Locate and identify every blood parasite.
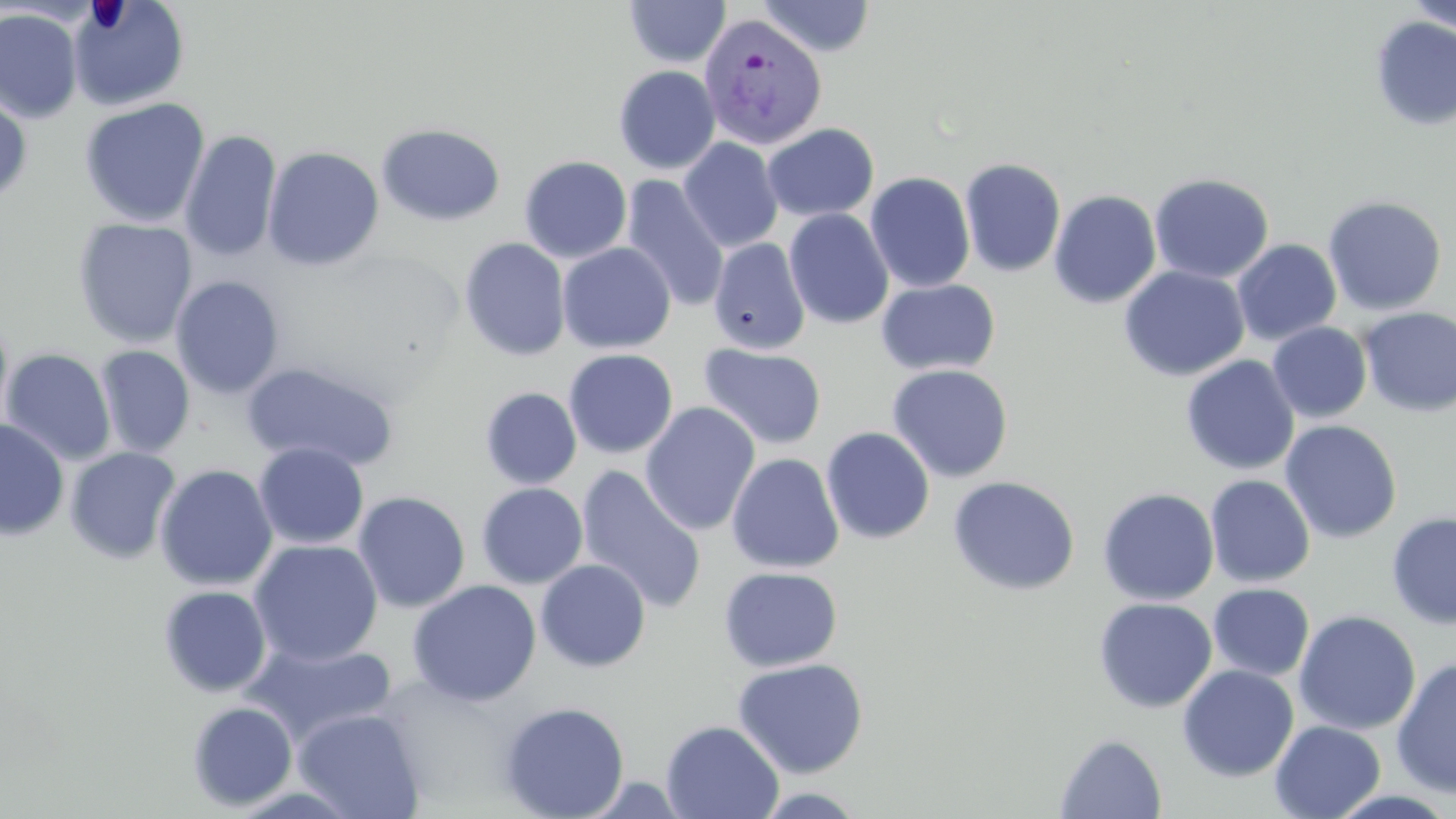
Approximate bounding boxes as (x1, y1, x2, y2) in pixels.
Plasmodium vivax-infected red blood cells: (699, 13, 828, 150).
No Plasmodium falciparum, Plasmodium ovale, Plasmodium malariae, Babesia divergens, or Trypanosoma brucei observed.

{
  "slide_level_diagnosis": "Plasmodium vivax",
  "magnification": "1000x",
  "modality": "optical microscopy",
  "uninfected_red_blood_cell_locations": "approximate bounding boxes as (x1, y1, x2, y2) in pixels: (69, 0, 190, 111), (757, 0, 876, 57), (625, 1, 730, 68), (1405, 2, 1456, 38), (0, 8, 82, 124), (1370, 16, 1456, 131), (613, 65, 721, 174), (0, 87, 33, 206), (79, 97, 211, 228), (762, 122, 878, 222), (376, 123, 506, 227), (180, 130, 282, 262), (679, 137, 784, 253), (262, 146, 385, 271), (519, 156, 632, 263), (959, 157, 1066, 278), (865, 171, 976, 293), (1149, 172, 1275, 284), (621, 175, 730, 311), (1048, 190, 1162, 309), (1322, 194, 1447, 316), (784, 208, 894, 330), (72, 218, 198, 348), (459, 237, 571, 361), (708, 237, 810, 355), (1232, 239, 1342, 346), (557, 242, 676, 354), (1119, 266, 1250, 381), (170, 275, 285, 399), (876, 278, 1000, 376), (1359, 307, 1456, 416), (0, 312, 14, 438), (1267, 322, 1372, 423), (698, 343, 827, 450), (95, 345, 195, 458), (1, 348, 116, 465), (563, 349, 678, 459), (1180, 355, 1300, 475), (240, 360, 400, 472), (886, 364, 1014, 483), (480, 387, 582, 490), (640, 402, 760, 536), (0, 418, 70, 541), (1280, 420, 1402, 544), (203, 426, 340, 570), (821, 426, 935, 545), (254, 442, 369, 550), (65, 446, 182, 564), (726, 453, 844, 574), (155, 464, 278, 591), (574, 466, 707, 614), (1205, 474, 1316, 588), (947, 475, 1081, 596), (476, 483, 588, 588), (1097, 487, 1220, 605), (353, 491, 471, 612), (1386, 511, 1455, 630), (249, 539, 383, 666), (535, 559, 651, 672), (719, 566, 843, 672), (406, 579, 542, 706), (1208, 582, 1315, 681), (158, 585, 272, 697), (1093, 597, 1217, 714), (1293, 610, 1421, 736), (242, 640, 398, 745), (1392, 657, 1456, 798), (732, 658, 869, 779), (1177, 664, 1299, 782), (187, 701, 298, 811), (498, 701, 630, 819), (292, 707, 426, 819), (660, 719, 784, 819), (1269, 720, 1386, 819), (1055, 733, 1168, 818), (751, 786, 870, 818)",
  "preparation": "thin blood smear",
  "stain": "May-Grünwald-Giemsa",
  "image_size": "1456×819 pixels",
  "field_of_view": "one of a larger specimen"
}